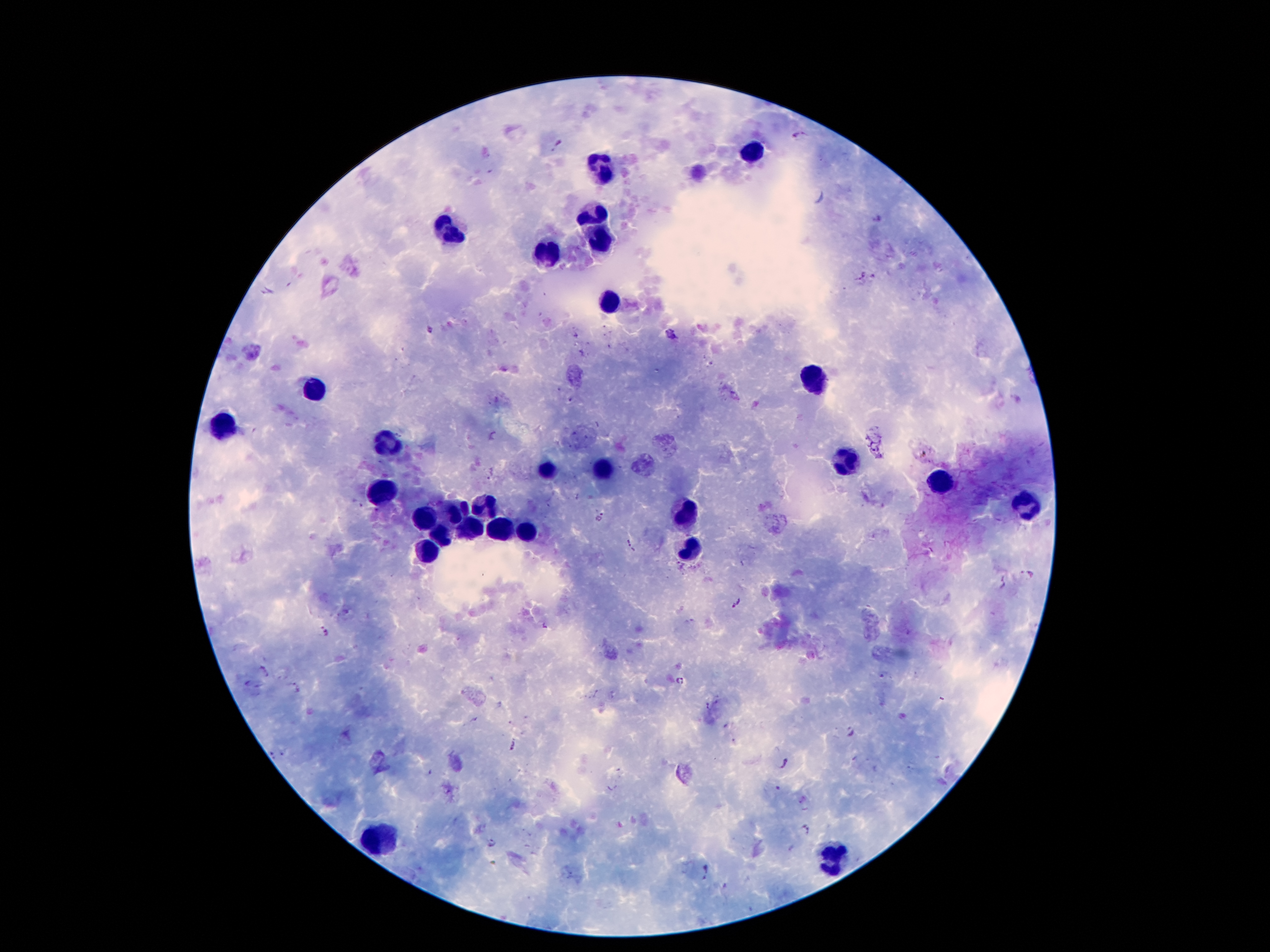
Approximate centers as [x, y] in pixels. Malaria parasite locations: [797, 133], [559, 146], [862, 274], [875, 278], [429, 329], [669, 334], [491, 473], [356, 503], [601, 517], [628, 546], [1026, 573], [737, 604], [324, 632], [264, 672], [679, 679], [296, 688], [850, 731], [512, 746], [784, 763], [806, 828], [493, 843], [706, 873]. Leukocyte locations: [751, 151], [605, 165], [596, 214], [445, 228], [598, 235], [546, 255], [609, 302], [814, 377], [317, 389], [224, 425], [385, 442], [848, 465], [602, 470], [546, 472], [940, 482], [385, 490], [1024, 505], [457, 507], [485, 507], [688, 512], [425, 515], [472, 528], [529, 529], [499, 531], [442, 533], [693, 552], [429, 553], [381, 836], [833, 857]. Thick blood film. Giemsa-stained preparation. Photographed through the microscope eyepiece with a smartphone camera. 100x magnification. Single field of view. Image is 1270×952 pixels. Patient malaria status: positive for Plasmodium falciparum.